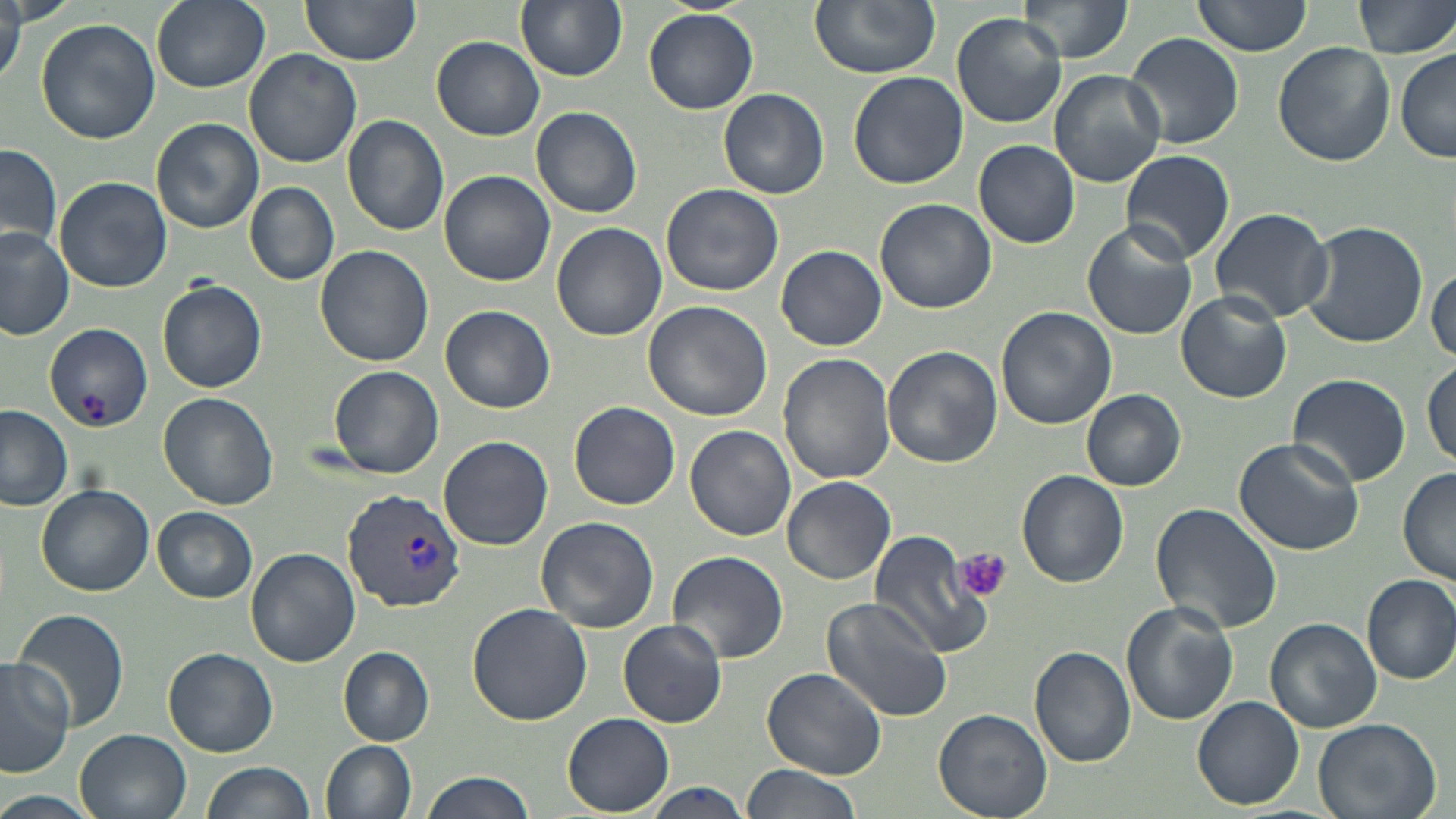
Approximate bounding boxes as (x1, y1, x2, y2) in pixels. Platelet locations: (955, 548, 1014, 602). Uninfected red blood cell locations: (152, 0, 270, 92), (299, 0, 421, 65), (517, 0, 627, 81), (810, 0, 941, 78), (1017, 0, 1130, 66), (1192, 0, 1312, 57), (1351, 0, 1456, 59), (0, 4, 25, 86), (644, 6, 758, 114), (952, 12, 1068, 128), (36, 19, 161, 143), (1126, 31, 1245, 149), (432, 36, 545, 141), (1273, 41, 1395, 167), (1046, 46, 1236, 167), (245, 48, 362, 168), (1394, 49, 1456, 163), (1049, 69, 1165, 187), (847, 70, 968, 190), (719, 88, 829, 199), (531, 107, 642, 217), (341, 114, 450, 237), (151, 118, 262, 235), (974, 140, 1080, 250), (1, 144, 61, 254), (1120, 150, 1233, 266), (439, 170, 556, 288), (54, 176, 173, 292), (661, 182, 784, 296), (245, 183, 339, 285), (875, 198, 995, 313), (1207, 206, 1336, 323), (1299, 220, 1428, 349), (551, 222, 667, 341), (1081, 223, 1199, 341), (0, 227, 75, 340), (776, 245, 887, 350), (315, 246, 433, 368), (1429, 262, 1455, 365), (157, 278, 268, 395), (1176, 290, 1291, 403), (643, 300, 773, 423), (441, 305, 556, 415), (995, 307, 1117, 430), (45, 324, 153, 431), (881, 345, 1002, 468), (778, 353, 896, 485), (1423, 360, 1456, 469), (327, 364, 445, 478), (1287, 373, 1412, 488), (1081, 389, 1187, 492), (157, 392, 279, 510), (569, 402, 679, 509), (0, 405, 74, 511), (685, 424, 797, 542), (439, 436, 553, 549), (1232, 438, 1363, 555), (1398, 468, 1456, 585), (1016, 470, 1128, 586), (782, 476, 896, 586), (37, 484, 154, 596), (1150, 502, 1282, 635), (153, 507, 259, 602), (536, 516, 659, 634), (866, 531, 991, 658), (245, 546, 359, 667), (666, 549, 790, 663), (1361, 573, 1456, 686), (820, 594, 955, 722), (1120, 601, 1239, 725), (467, 602, 593, 724), (10, 608, 129, 735), (1265, 617, 1382, 732), (617, 619, 729, 728), (1030, 646, 1136, 767), (163, 647, 277, 758), (337, 648, 435, 744), (0, 655, 74, 778), (973, 664, 1126, 794), (762, 667, 888, 781), (1192, 694, 1305, 809), (934, 707, 1053, 818), (563, 712, 673, 816), (1312, 717, 1441, 819), (76, 728, 193, 818), (320, 740, 417, 819), (202, 761, 316, 819), (740, 765, 865, 819), (419, 770, 538, 819), (642, 782, 755, 818), (0, 791, 100, 819). Plasmodium vivax-infected red blood cell locations: (343, 488, 467, 614). Slide-level diagnosis: Plasmodium vivax. Captured at 1000x magnification. May-Grünwald-Giemsa-stained preparation. Thin blood film. Light microscopy. Image is 1456×819 pixels. Single field of view.